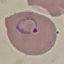

result: malaria parasites detected
preparation: thin blood film
image_type: automatically extracted cell patch, resized to 64 × 64 pixels
stain: Giemsa
capture: smartphone through the microscope eyepiece